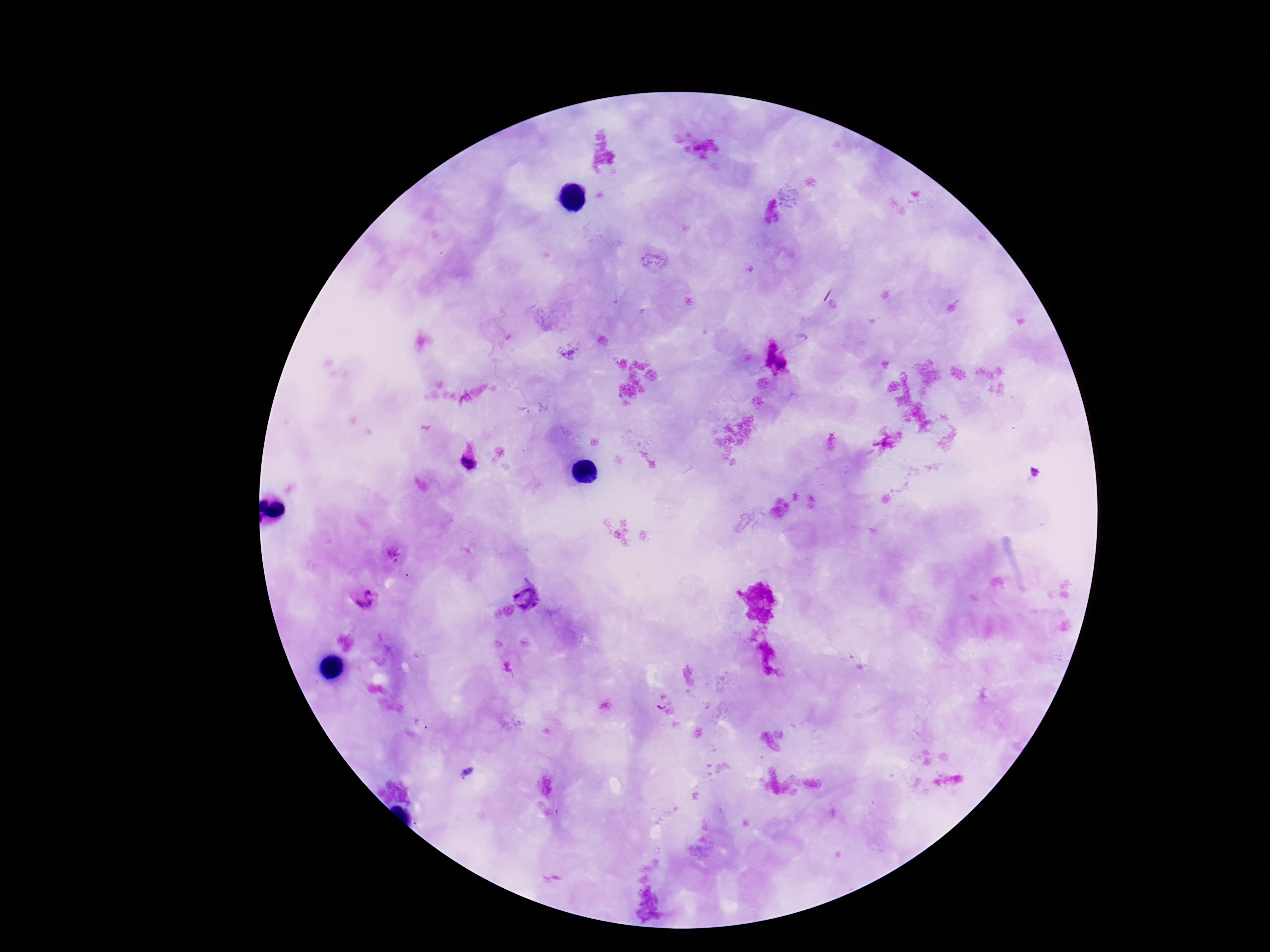
Approximate centers as {x, y} in pixels. Plasmodium parasite locations: {468, 462}, {527, 597}, {367, 601}. Giemsa-stained preparation. Single field of view. Photographed through the microscope eyepiece with a smartphone camera. Image is 1270×952 pixels. 100x magnification. Patient malaria status: infected. Thick peripheral-blood smear.